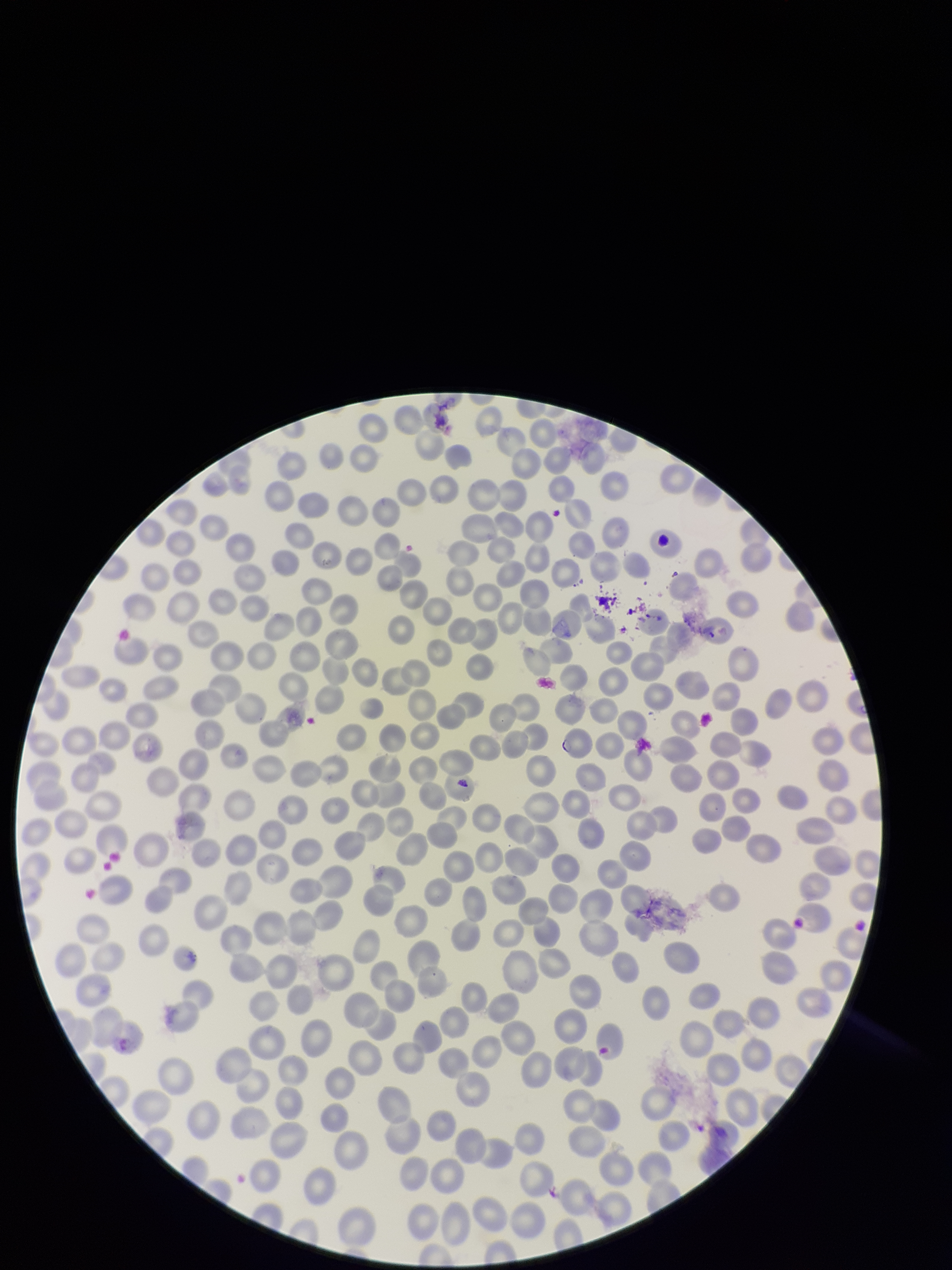
preparation = thin smear
parasitized red blood cells = none detected
species reported for this patient = Plasmodium falciparum
parasitized red blood cell count = 0
patient malaria status = positive
red blood cell count = 312
capture = smartphone photograph through the microscope eyepiece
image size = 952×1270 pixels
stain = Giemsa
field of view = single